Identify the parasite.
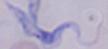
This is a trypanosome.

{
  "magnification": "1000x",
  "modality": "micrograph"
}